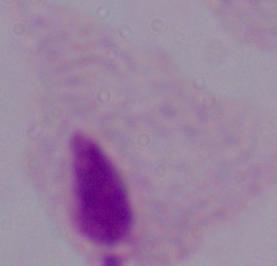
magnification = 1000x
identification = trichomonad
modality = micrograph